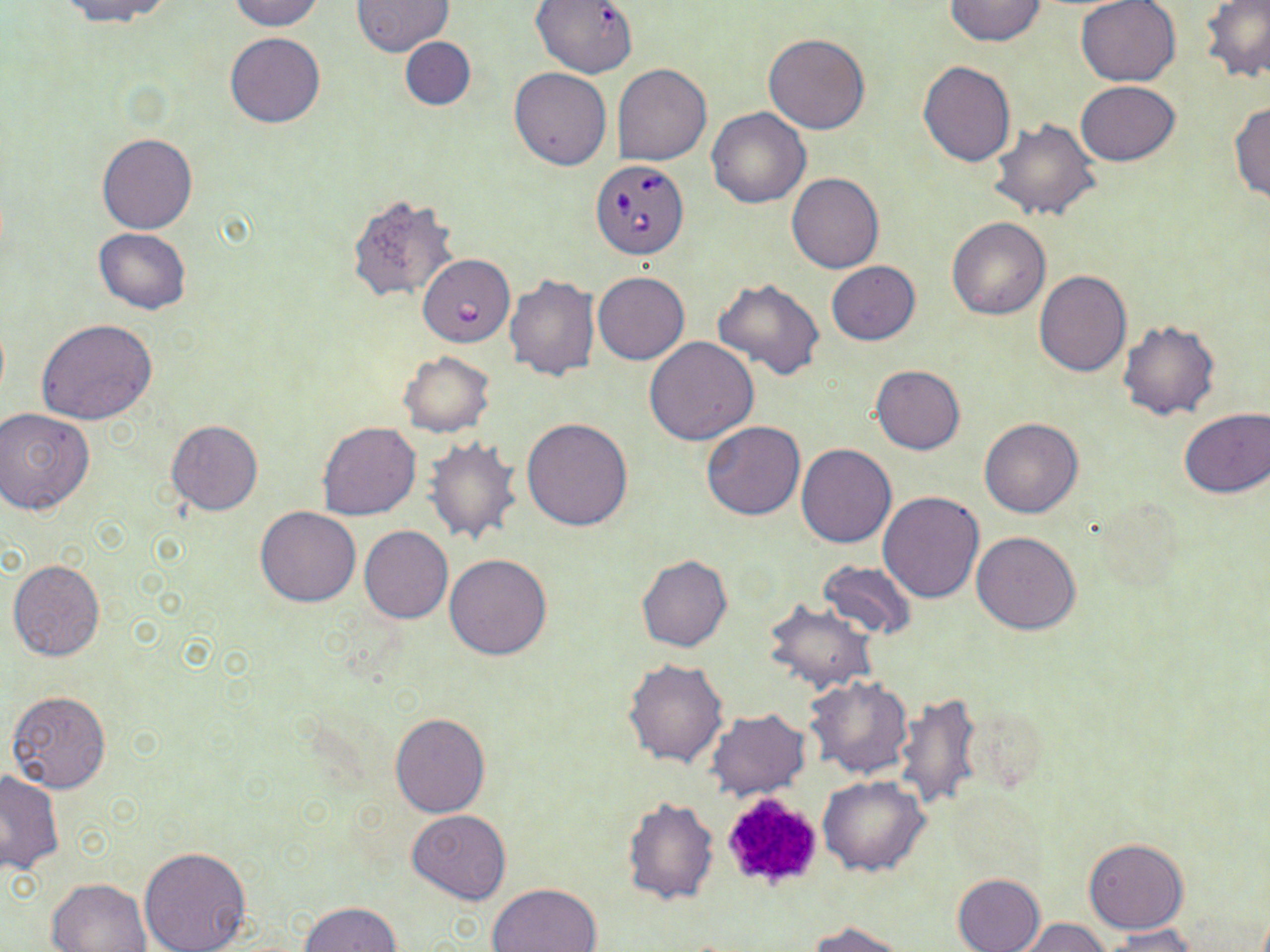

Summary:
  - Coordinate format: approximate bounding boxes as (x1,y1)-(x2,y2) corner pairs in pixels
  - Platelet locations: (717,792)-(825,893)
  - Uninfected red blood cell locations: (60,0)-(178,25), (229,0)-(324,31), (353,0)-(452,55), (944,0)-(1048,46), (1075,0)-(1183,86), (531,1)-(638,78), (1199,1)-(1270,83), (225,32)-(324,127), (764,33)-(870,134), (400,37)-(475,112), (918,60)-(1017,167), (612,64)-(712,165), (509,67)-(612,170), (1076,81)-(1180,165), (1231,100)-(1270,203), (706,107)-(810,208), (988,117)-(1102,222), (97,134)-(197,234), (786,173)-(884,274), (347,195)-(460,304), (947,216)-(1051,320), (94,228)-(191,314), (827,261)-(920,345), (1034,269)-(1132,376), (592,271)-(689,364), (504,274)-(600,380), (712,277)-(826,381), (36,320)-(159,426), (1118,320)-(1220,420), (644,338)-(759,445), (399,351)-(496,436), (870,365)-(965,454), (0,407)-(95,516), (1178,408)-(1269,499), (522,417)-(634,530), (165,419)-(262,516), (979,419)-(1084,518), (701,421)-(805,520), (317,422)-(421,521), (424,437)-(522,545), (796,444)-(896,548), (878,491)-(984,604), (256,506)-(361,607), (360,526)-(453,624), (971,531)-(1081,634), (445,554)-(551,660), (636,554)-(733,652), (8,559)-(105,661), (818,562)-(917,640), (763,598)-(877,692), (623,657)-(728,767), (805,674)-(914,778), (6,690)-(111,794), (891,690)-(984,814), (704,709)-(809,800), (390,713)-(490,817), (1,769)-(63,874), (818,775)-(928,876), (623,794)-(719,905), (407,809)-(511,904), (1084,837)-(1188,933), (138,847)-(252,952), (951,873)-(1046,952), (45,877)-(152,951), (487,881)-(603,952), (297,902)-(403,952), (1018,918)-(1109,952), (807,920)-(910,951), (1102,925)-(1202,951)
  - Babesia divergens-infected red blood cell locations: (590,160)-(690,260), (420,256)-(509,349)
  - Slide-level diagnosis: Babesia divergens
  - Field of view: one of a larger specimen
  - Modality: optical microscopy
  - Preparation: thin blood film
  - Magnification: 1000x
  - Stain: May-Grünwald-Giemsa
  - Image size: 1270×952 pixels